Assess this cell for malaria.
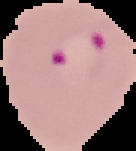
Parasitized.

The area outside the segmented cell region is set to black. From a thin blood film. Image is 136×151 pixels.